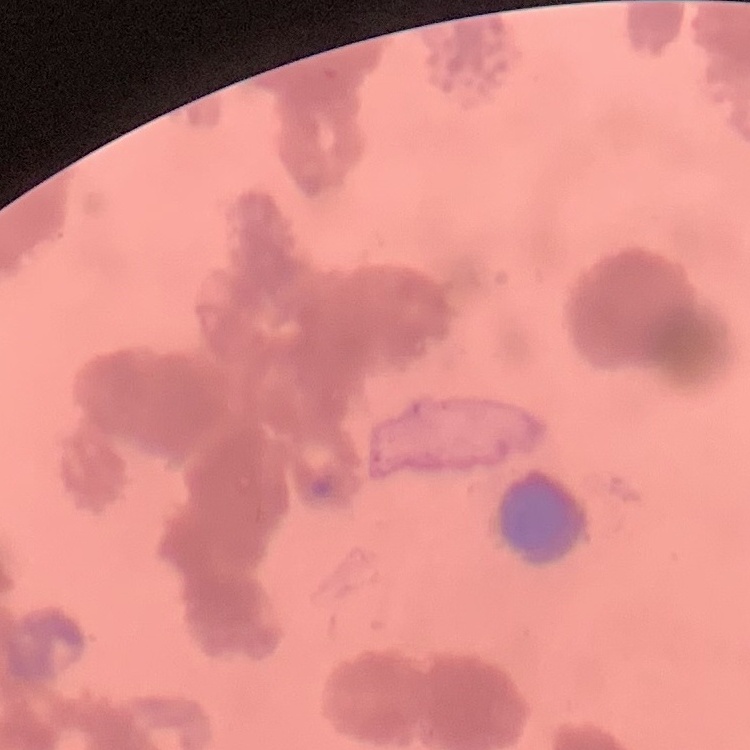
{
  "erythrocyte_morphology": "rouleaux formation",
  "stain": "Field's or Giemsa",
  "preparation": "thin peripheral smear",
  "image_type": "square crop of a larger photomicrograph"
}